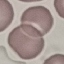

result = negative for malaria parasites
capture = smartphone through the microscope eyepiece
preparation = thin blood film
image type = cell patch, automatically extracted from a larger field of view and resized to 64 × 64 pixels
stain = Giemsa